Assess this cell for malaria.
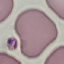
Uninfected.

Automatically extracted cell patch, resized to 64 × 64 pixels. Giemsa stain. Photographed with a smartphone camera at the microscope eyepiece. Thin blood smear.